Give the position of every malaria parasite.
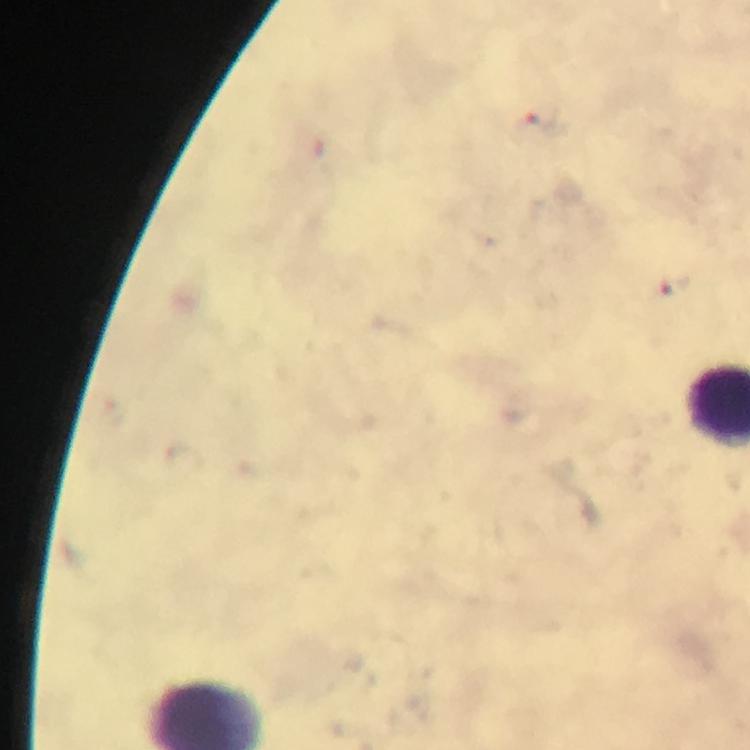
Approximate centers as [x, y] in pixels.
Malaria parasites: [543, 120], [671, 285].

magnification = 100x
image size = 750×750 pixels
context = from a malaria diagnostic workup
stain = Giemsa
cropped from = one field of view
capture = smartphone mounted on the microscope
preparation = thick blood smear
immersion oil = applied